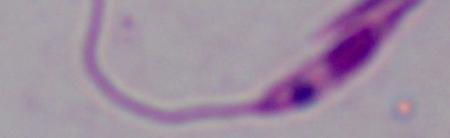
identification = Leishmania
modality = photomicrograph
magnification = 1000x